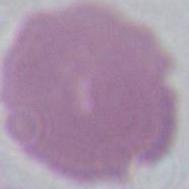

identification = red blood cell
magnification = 1000x
modality = micrograph